Locate every blood parasite and identify its species.
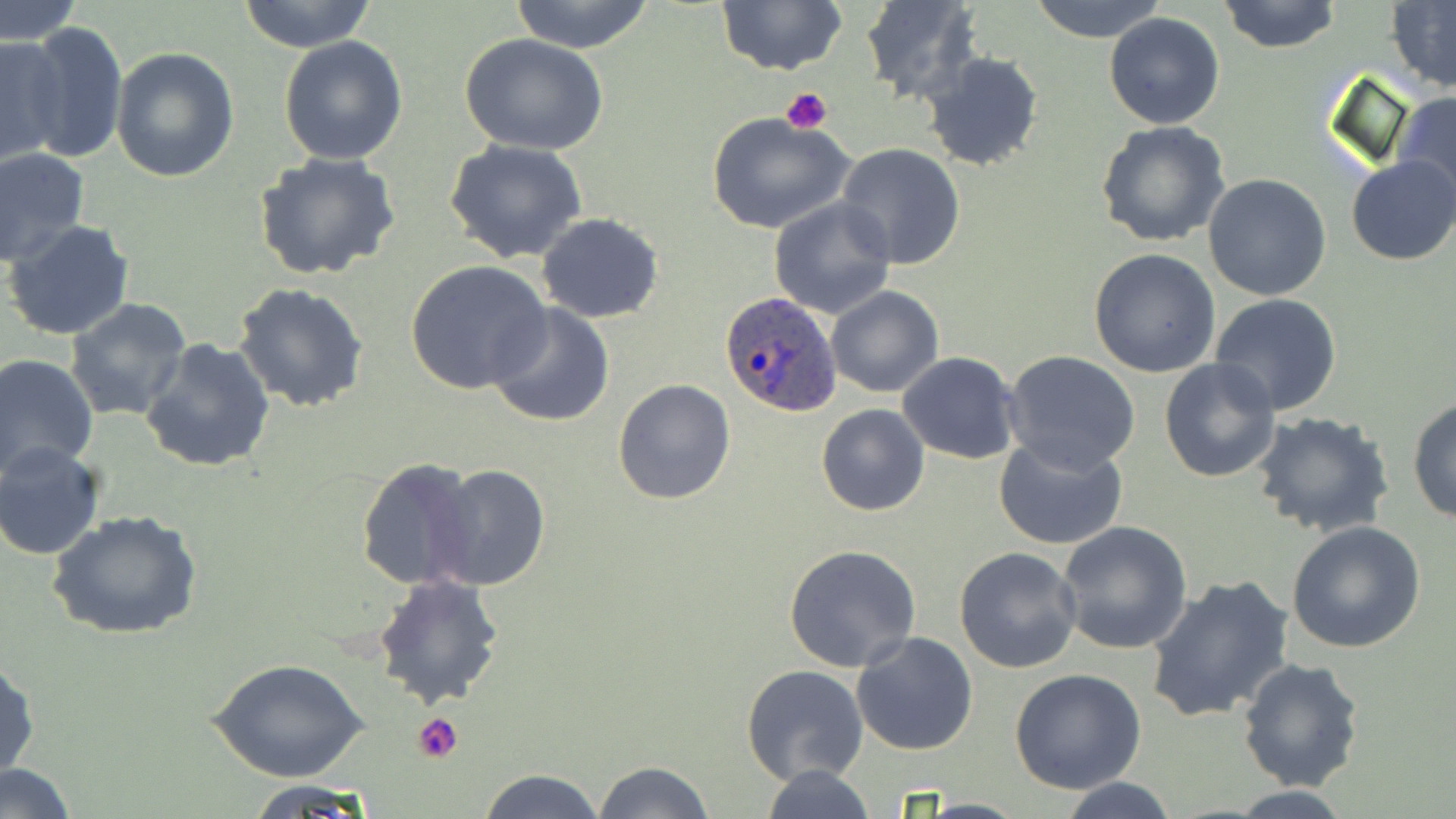
Approximate bounding boxes as (x1,y1)-(x2,y2) corner pairs in pixels.
Plasmodium ovale-infected red blood cells: (720,292)-(843,417).
No Plasmodium falciparum, Plasmodium malariae, Plasmodium vivax, Babesia divergens, or Trypanosoma brucei observed.

slide_level_diagnosis: Plasmodium ovale
platelet_locations: 'approximate bounding boxes as (x1,y1)-(x2,y2) corner pairs in pixels: (780,86)-(834,135), (409,711)-(466,763)'
magnification: 1000x
preparation: thin blood smear
field_of_view: one of a larger specimen
uninfected_red_blood_cell_locations: 'approximate bounding boxes as (x1,y1)-(x2,y2) corner pairs in pixels: (0,0)-(82,45), (238,0)-(378,52), (509,0)-(656,52), (718,0)-(847,75), (862,0)-(983,105), (1028,0)-(1170,43), (1217,0)-(1344,54), (1386,2)-(1456,94), (1103,12)-(1225,129), (20,20)-(127,165), (0,35)-(69,167), (460,35)-(608,155), (278,36)-(408,165), (111,45)-(239,183), (921,51)-(1045,173), (1393,91)-(1456,211), (707,112)-(855,235), (1096,121)-(1231,248), (444,140)-(590,263), (835,144)-(967,269), (0,146)-(90,266), (254,153)-(403,283), (1347,156)-(1456,266), (1203,174)-(1333,301), (768,196)-(897,320), (537,213)-(665,323), (4,219)-(135,341), (1088,249)-(1221,377), (405,260)-(553,397), (233,282)-(369,413), (825,286)-(944,398), (1209,293)-(1344,416), (64,297)-(194,423), (485,301)-(617,428), (139,338)-(277,473), (1003,349)-(1141,473), (896,352)-(1020,463), (1,353)-(99,476), (1159,358)-(1283,483), (612,378)-(738,505), (1408,395)-(1456,525), (816,404)-(929,516), (1251,412)-(1395,538), (993,436)-(1128,554), (0,441)-(106,561), (353,459)-(481,592), (429,464)-(553,590), (48,508)-(203,640), (1285,519)-(1428,654), (1055,520)-(1194,654), (783,544)-(921,672), (953,546)-(1083,673), (371,574)-(506,709), (1144,574)-(1295,725), (851,632)-(980,756), (1,657)-(39,785), (1237,658)-(1367,792), (209,659)-(369,782), (741,665)-(870,786), (1012,667)-(1146,793), (593,759)-(718,818), (2,763)-(77,817), (756,764)-(881,819), (476,768)-(605,819), (1057,778)-(1183,818), (245,779)-(378,815), (1221,786)-(1363,817)'
image_size: 1456×819 pixels
stain: May-Grünwald-Giemsa
modality: optical microscopy